Give the extent of all Trypanosoma brucei.
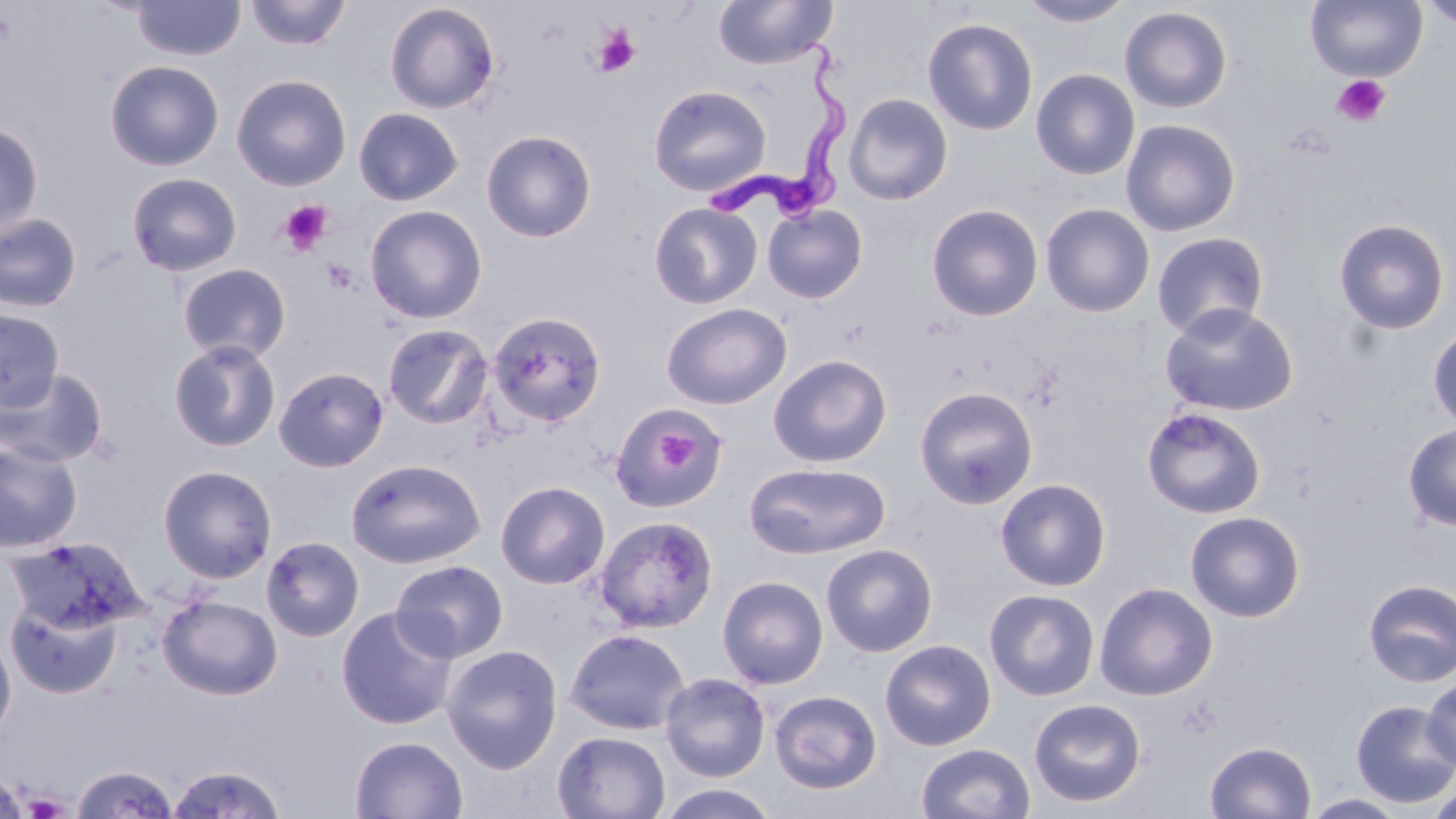

Approximate bounding boxes as [x1, y1, x2, y2] in pixels.
Trypanosoma brucei: [701, 25, 853, 229].

Summary:
  - Uninfected red blood cell locations: [132, 0, 244, 61], [245, 0, 351, 51], [712, 0, 837, 70], [1018, 0, 1134, 27], [1305, 0, 1427, 82], [1418, 0, 1456, 30], [384, 2, 500, 114], [1119, 6, 1233, 113], [922, 17, 1038, 135], [104, 59, 224, 171], [1030, 68, 1140, 180], [231, 73, 351, 191], [648, 85, 771, 197], [843, 93, 953, 205], [354, 107, 464, 206], [1120, 118, 1240, 236], [0, 121, 44, 238], [481, 129, 597, 243], [126, 172, 242, 276], [649, 202, 762, 309], [762, 203, 868, 304], [926, 203, 1044, 321], [1040, 203, 1155, 318], [365, 205, 487, 323], [0, 212, 83, 313], [1333, 218, 1450, 335], [1151, 231, 1270, 340], [178, 263, 291, 362], [661, 302, 792, 409], [1159, 303, 1299, 417], [0, 307, 65, 412], [486, 311, 607, 428], [382, 323, 495, 429], [1427, 323, 1456, 430], [168, 338, 281, 452], [768, 354, 892, 468], [273, 366, 389, 472], [0, 367, 110, 468], [915, 386, 1038, 509], [609, 402, 727, 513], [1142, 406, 1266, 519], [1402, 423, 1456, 530], [0, 440, 82, 552], [346, 458, 485, 570], [744, 462, 891, 559], [157, 464, 277, 583], [995, 478, 1112, 591], [495, 480, 610, 589], [1184, 510, 1305, 622], [593, 515, 719, 633], [261, 536, 364, 642], [4, 537, 149, 635], [821, 543, 938, 657], [390, 559, 510, 663], [716, 575, 828, 689], [1362, 578, 1456, 686], [1094, 582, 1218, 701], [984, 589, 1100, 701], [157, 594, 282, 700], [6, 597, 122, 698], [336, 606, 458, 730], [564, 628, 690, 735], [0, 629, 16, 745], [880, 639, 996, 751], [442, 644, 563, 773], [660, 673, 770, 782], [1421, 674, 1456, 772], [768, 689, 882, 794], [1028, 698, 1147, 807], [1350, 699, 1456, 808], [552, 731, 671, 818], [350, 735, 468, 818], [1205, 741, 1316, 819], [916, 743, 1035, 819], [165, 763, 288, 818], [70, 764, 181, 818], [0, 767, 28, 819], [1425, 781, 1456, 819], [655, 784, 781, 819], [1300, 793, 1409, 818]
  - Platelet locations: [592, 24, 641, 77], [1331, 74, 1391, 127], [280, 200, 332, 256], [320, 257, 360, 294], [657, 430, 700, 473]
  - Slide-level diagnosis: Trypanosoma brucei
  - Image size: 1456×819 pixels
  - Magnification: 1000x
  - Stain: May-Grünwald-Giemsa
  - Modality: light microscopy
  - Field of view: one of a larger specimen
  - Preparation: thin blood film